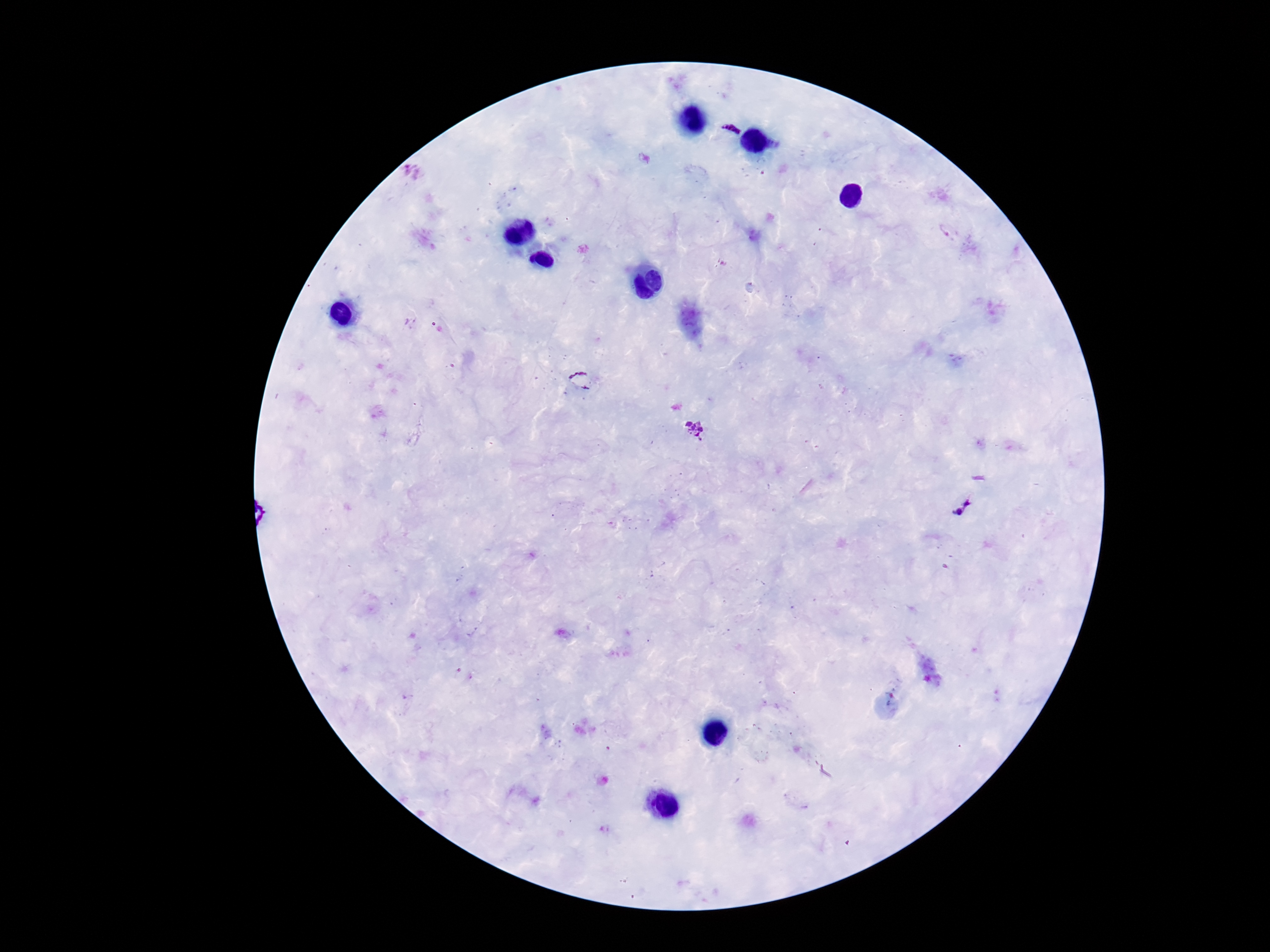

field of view = single
image size = 1270×952 pixels
capture = smartphone camera through the microscope eyepiece
Plasmodium parasite locations = approximate centers as [x, y] in pixels: [729, 128], [580, 380], [695, 428], [964, 504]
patient malaria status = positive
magnification = 100x
stain = Giemsa
preparation = thick blood smear